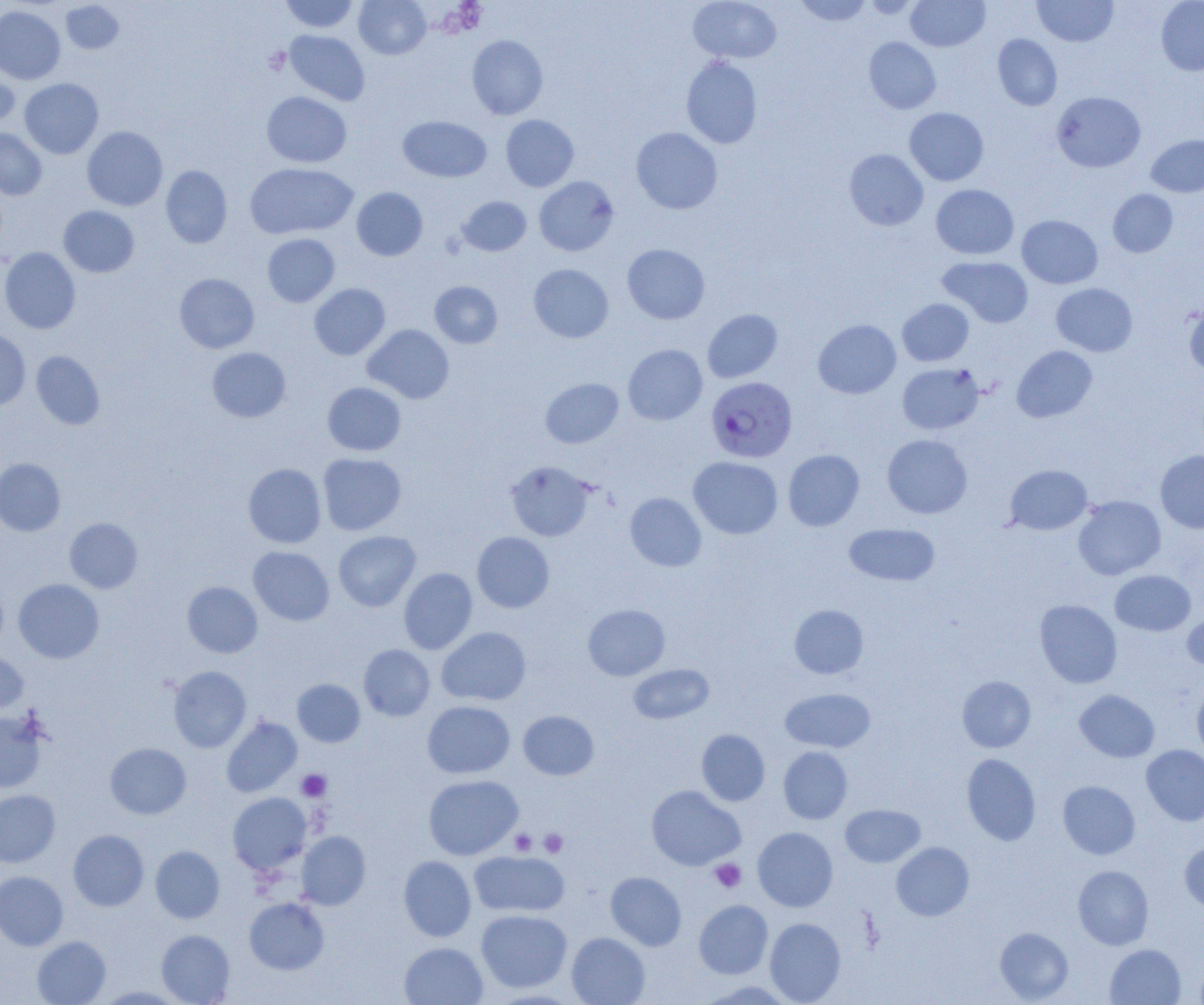

Approximate bounding boxes as named x1/y1/x2/y2 corners in pixels. Platelet locations: (x1=297, y1=769, x2=331, y2=802), (x1=539, y1=828, x2=568, y2=857), (x1=510, y1=830, x2=536, y2=855), (x1=710, y1=859, x2=746, y2=892). Uninfected red blood cell locations: (x1=280, y1=0, x2=359, y2=32), (x1=354, y1=0, x2=431, y2=59), (x1=688, y1=0, x2=781, y2=63), (x1=793, y1=0, x2=871, y2=26), (x1=860, y1=0, x2=922, y2=19), (x1=906, y1=0, x2=990, y2=52), (x1=1033, y1=0, x2=1118, y2=47), (x1=1156, y1=0, x2=1204, y2=76), (x1=61, y1=1, x2=125, y2=54), (x1=0, y1=6, x2=65, y2=84), (x1=284, y1=30, x2=369, y2=105), (x1=992, y1=34, x2=1062, y2=111), (x1=467, y1=35, x2=548, y2=119), (x1=864, y1=37, x2=941, y2=114), (x1=681, y1=56, x2=763, y2=149), (x1=0, y1=70, x2=20, y2=132), (x1=20, y1=78, x2=103, y2=159), (x1=262, y1=91, x2=351, y2=168), (x1=1052, y1=91, x2=1145, y2=172), (x1=904, y1=107, x2=988, y2=186), (x1=501, y1=115, x2=579, y2=191), (x1=398, y1=116, x2=491, y2=182), (x1=82, y1=126, x2=167, y2=211), (x1=631, y1=127, x2=722, y2=214), (x1=0, y1=129, x2=47, y2=200), (x1=1146, y1=134, x2=1204, y2=197), (x1=845, y1=149, x2=928, y2=230), (x1=246, y1=163, x2=357, y2=239), (x1=161, y1=165, x2=232, y2=248), (x1=534, y1=176, x2=619, y2=256), (x1=931, y1=184, x2=1019, y2=259), (x1=352, y1=187, x2=427, y2=261), (x1=1108, y1=189, x2=1178, y2=257), (x1=457, y1=196, x2=531, y2=256), (x1=58, y1=205, x2=139, y2=277), (x1=1017, y1=215, x2=1102, y2=289), (x1=262, y1=234, x2=339, y2=307), (x1=622, y1=243, x2=710, y2=324), (x1=0, y1=247, x2=81, y2=334), (x1=938, y1=256, x2=1033, y2=328), (x1=529, y1=264, x2=613, y2=342), (x1=174, y1=273, x2=259, y2=353), (x1=430, y1=281, x2=502, y2=348), (x1=309, y1=283, x2=390, y2=360), (x1=1051, y1=283, x2=1138, y2=356), (x1=897, y1=299, x2=974, y2=366), (x1=1184, y1=304, x2=1204, y2=376), (x1=703, y1=309, x2=782, y2=383), (x1=813, y1=319, x2=901, y2=398), (x1=363, y1=324, x2=454, y2=404), (x1=0, y1=329, x2=30, y2=410), (x1=623, y1=344, x2=707, y2=425), (x1=1012, y1=346, x2=1097, y2=422), (x1=207, y1=347, x2=291, y2=422), (x1=31, y1=351, x2=105, y2=429), (x1=897, y1=363, x2=983, y2=434), (x1=540, y1=378, x2=623, y2=448), (x1=323, y1=382, x2=406, y2=456), (x1=882, y1=434, x2=972, y2=518), (x1=783, y1=449, x2=864, y2=530), (x1=1155, y1=450, x2=1204, y2=533), (x1=318, y1=453, x2=406, y2=535), (x1=689, y1=456, x2=782, y2=539), (x1=0, y1=458, x2=65, y2=536), (x1=505, y1=461, x2=595, y2=541), (x1=243, y1=463, x2=326, y2=548), (x1=1005, y1=464, x2=1092, y2=535), (x1=625, y1=492, x2=706, y2=571), (x1=1073, y1=495, x2=1165, y2=580), (x1=64, y1=517, x2=142, y2=593), (x1=844, y1=523, x2=940, y2=587), (x1=333, y1=531, x2=420, y2=611), (x1=472, y1=532, x2=554, y2=613), (x1=248, y1=546, x2=334, y2=626), (x1=399, y1=568, x2=477, y2=654), (x1=1110, y1=570, x2=1196, y2=636), (x1=13, y1=579, x2=104, y2=663), (x1=182, y1=581, x2=262, y2=658), (x1=1034, y1=599, x2=1122, y2=688), (x1=583, y1=604, x2=669, y2=680), (x1=789, y1=604, x2=868, y2=679), (x1=1182, y1=612, x2=1204, y2=672), (x1=437, y1=626, x2=531, y2=706), (x1=359, y1=644, x2=435, y2=720), (x1=0, y1=647, x2=28, y2=712), (x1=628, y1=663, x2=714, y2=724), (x1=168, y1=666, x2=251, y2=752), (x1=957, y1=676, x2=1036, y2=752), (x1=292, y1=679, x2=365, y2=747), (x1=1192, y1=682, x2=1204, y2=760), (x1=780, y1=688, x2=875, y2=752), (x1=1074, y1=690, x2=1159, y2=762), (x1=422, y1=700, x2=514, y2=778), (x1=518, y1=710, x2=599, y2=780), (x1=0, y1=711, x2=48, y2=793), (x1=221, y1=717, x2=302, y2=797), (x1=696, y1=729, x2=770, y2=806), (x1=105, y1=743, x2=191, y2=819), (x1=1142, y1=745, x2=1204, y2=826), (x1=778, y1=746, x2=852, y2=824), (x1=962, y1=753, x2=1041, y2=845), (x1=423, y1=775, x2=523, y2=860), (x1=1058, y1=781, x2=1140, y2=859), (x1=646, y1=785, x2=745, y2=870), (x1=0, y1=790, x2=60, y2=867), (x1=228, y1=793, x2=311, y2=874), (x1=840, y1=804, x2=925, y2=867), (x1=753, y1=827, x2=838, y2=912), (x1=68, y1=830, x2=149, y2=911), (x1=296, y1=831, x2=371, y2=910), (x1=891, y1=842, x2=974, y2=920), (x1=1180, y1=842, x2=1204, y2=915), (x1=150, y1=845, x2=224, y2=923), (x1=469, y1=851, x2=569, y2=917), (x1=399, y1=856, x2=476, y2=942), (x1=1073, y1=865, x2=1153, y2=949), (x1=0, y1=871, x2=68, y2=950), (x1=606, y1=872, x2=686, y2=950), (x1=244, y1=897, x2=329, y2=974), (x1=694, y1=900, x2=773, y2=978), (x1=476, y1=909, x2=572, y2=992), (x1=764, y1=918, x2=846, y2=1004), (x1=995, y1=927, x2=1073, y2=1003), (x1=156, y1=929, x2=235, y2=1004), (x1=567, y1=932, x2=650, y2=1005), (x1=32, y1=936, x2=111, y2=1005), (x1=399, y1=942, x2=487, y2=1005), (x1=1105, y1=944, x2=1186, y2=1005), (x1=697, y1=980, x2=797, y2=1004), (x1=96, y1=986, x2=188, y2=1004). Plasmodium falciparum-infected red blood cell locations: (x1=706, y1=377, x2=797, y2=463). Slide-level diagnosis: Plasmodium falciparum. Image is 1204×1005 pixels. Light microscopy. Thin blood smear. Single field of view. Captured at 1000x magnification.